Give the position of every leukocyte visible.
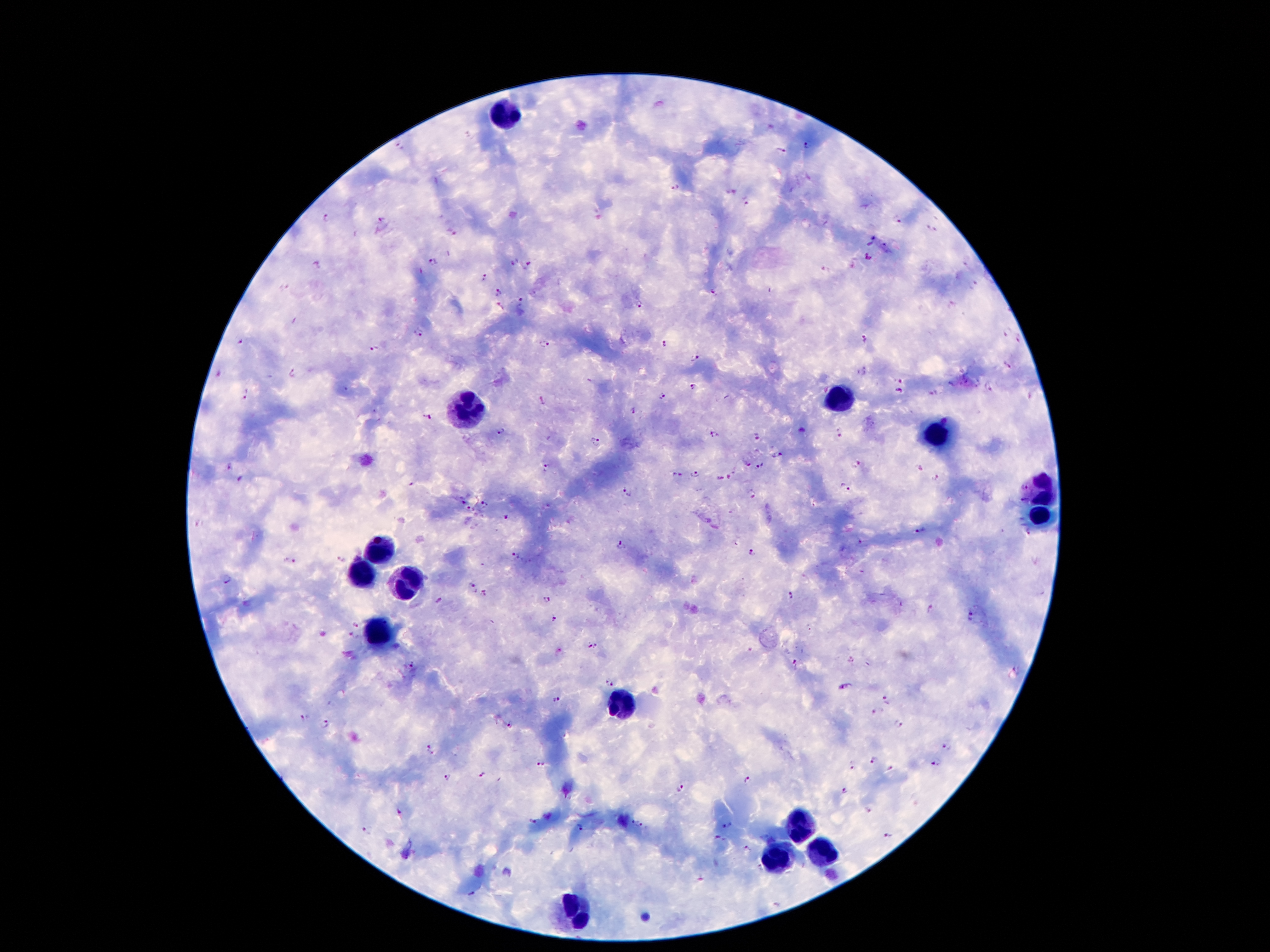

Approximate centers as [x, y] in pixels.
Leukocytes: [505, 116], [839, 397], [465, 408], [932, 436], [1039, 488], [1039, 522], [383, 545], [360, 576], [410, 585], [383, 638], [621, 708], [798, 826], [821, 851], [776, 860], [571, 914].

Summary:
  - Malaria parasite locations: [401, 146], [806, 146], [781, 151], [675, 186], [731, 192], [746, 203], [329, 217], [381, 220], [897, 221], [930, 229], [451, 232], [875, 235], [867, 245], [885, 248], [870, 257], [513, 260], [431, 261], [528, 264], [317, 266], [966, 268], [827, 270], [484, 278], [973, 284], [770, 289], [712, 291], [497, 292], [521, 300], [639, 305], [951, 305], [500, 308], [418, 331], [1005, 332], [864, 339], [1018, 339], [241, 343], [544, 343], [665, 343], [373, 349], [695, 357], [1007, 365], [863, 371], [294, 372], [900, 380], [693, 386], [988, 389], [346, 390], [899, 391], [933, 393], [246, 394], [662, 396], [1030, 396], [542, 400], [635, 412], [428, 417], [803, 430], [501, 431], [713, 433], [842, 433], [756, 436], [595, 441], [776, 455], [229, 464], [746, 464], [856, 465], [759, 466], [547, 468], [693, 473], [676, 475], [720, 477], [730, 477], [240, 479], [935, 480], [411, 483], [846, 487], [1021, 488], [627, 492], [753, 494], [1021, 499], [464, 500], [486, 505], [470, 512], [507, 517], [200, 523], [919, 530], [1026, 535], [861, 542], [622, 545], [753, 552], [516, 556], [342, 559], [290, 560], [861, 572], [228, 579], [473, 590], [486, 594], [790, 594], [439, 600], [547, 600], [930, 607], [973, 615], [555, 619], [355, 626], [352, 636], [594, 646], [557, 652], [850, 659], [413, 662], [796, 663], [610, 682], [846, 687], [887, 699], [558, 701], [877, 713], [303, 718], [326, 724], [511, 724], [897, 724], [946, 747], [431, 751], [875, 760], [937, 761], [542, 765], [850, 766], [889, 771], [483, 773], [445, 776], [747, 780], [681, 789], [845, 791], [869, 809], [399, 813], [534, 822], [728, 823], [638, 824], [580, 828], [366, 830], [888, 835], [760, 836], [773, 836], [720, 838], [747, 849], [758, 867], [701, 879], [471, 894], [778, 906]
  - Field of view: one from this slide
  - Stain: Giemsa
  - Image size: 1270×952 pixels
  - Capture: smartphone through the microscope eyepiece
  - Patient malaria status: positive for Plasmodium falciparum
  - Magnification: 100x
  - Preparation: thick peripheral-blood smear